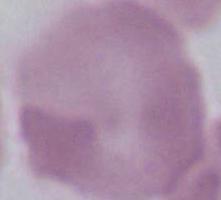

modality: micrograph
magnification: 1000x
identification: erythrocyte